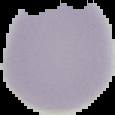

image size = 115×115 pixels
preparation = thin blood film
result = negative for malaria parasites
image type = cell region segmented out of the field of view; surrounding area masked to black